Give the preparation type.
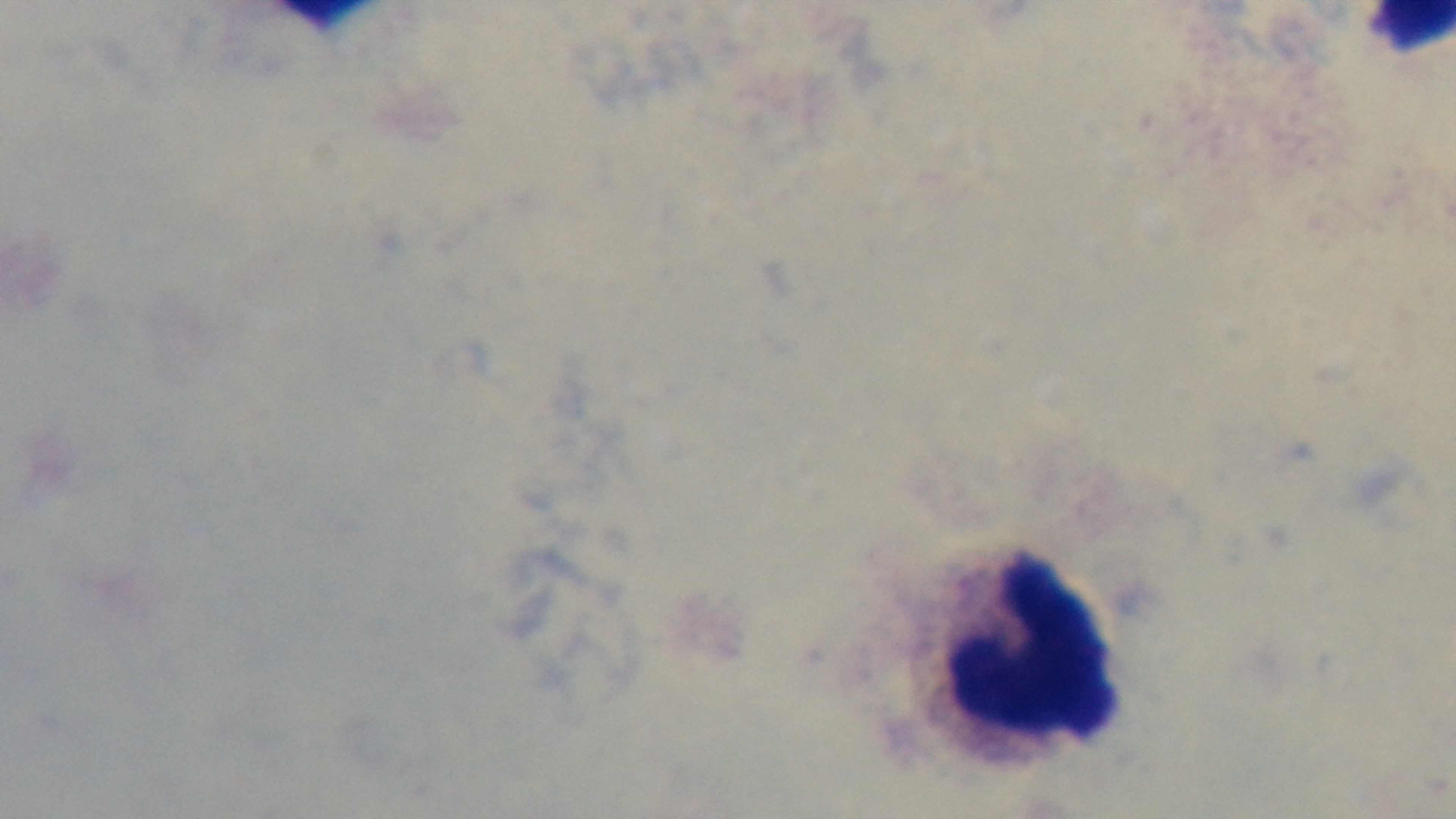
It is a thick blood film.

modality = light microscopy
field of view = single
objective = 100x oil immersion
capture = mounted 4K digital camera
malaria status = negative
stain = Giemsa